Name the blood parasite species.
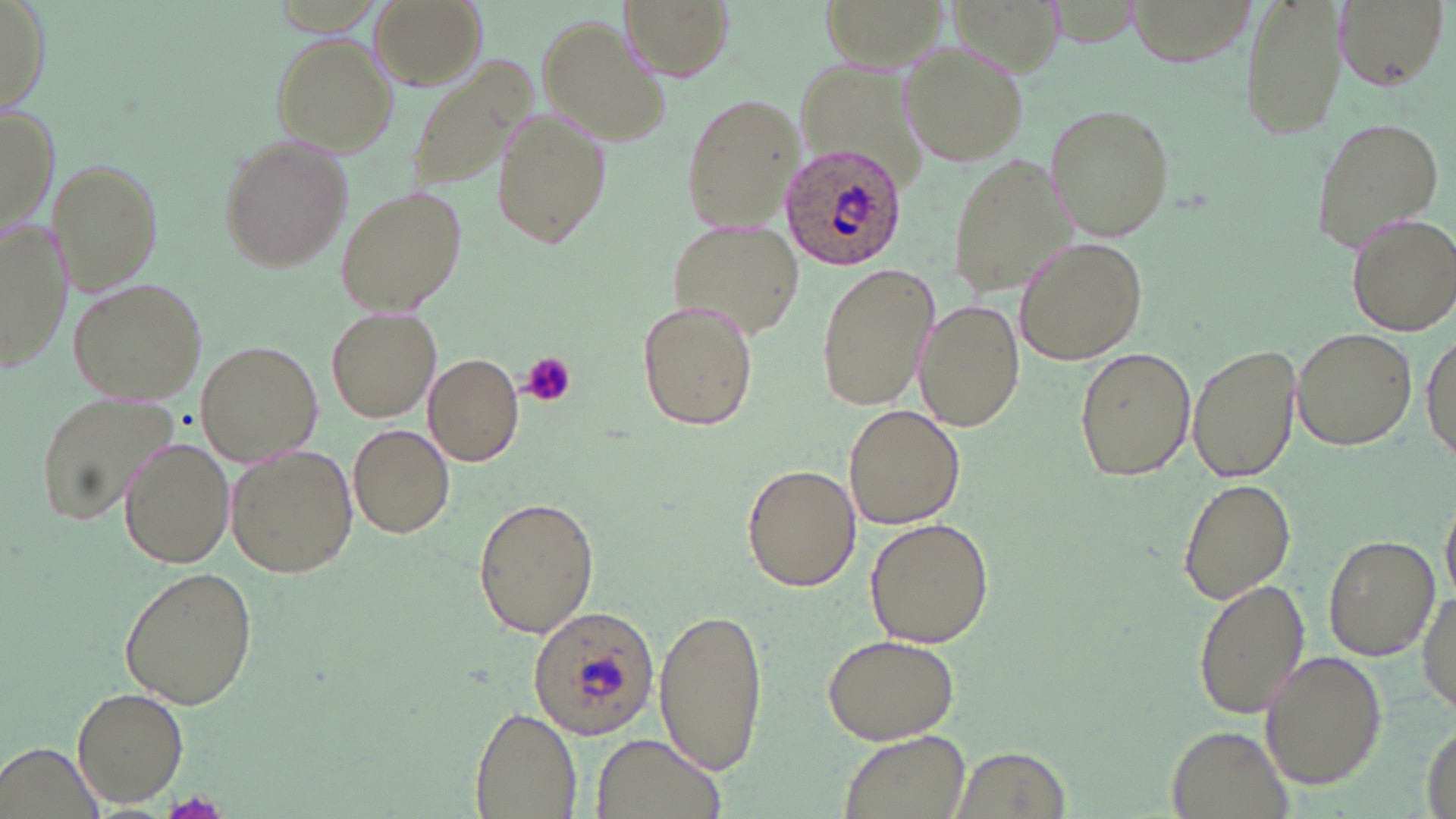
Plasmodium ovale.

magnification = 1000x
modality = light microscopy
platelet locations = approximate bounding boxes as (x1,y1)-(x2,y2) corner pairs in pixels: (521,352)-(576,408)
image size = 1456×819 pixels
stain = May-Grünwald-Giemsa
Plasmodium ovale-infected red blood cell locations = approximate bounding boxes as (x1,y1)-(x2,y2) corner pairs in pixels: (780,144)-(907,271), (526,605)-(658,738)
field of view = one of a larger specimen
uninfected red blood cell locations = approximate bounding boxes as (x1,y1)-(x2,y2) corner pairs in pixels: (369,0)-(484,91), (621,0)-(731,80), (822,0)-(951,69), (1238,0)-(1348,143), (1332,0)-(1449,91), (0,2)-(50,117), (540,15)-(669,142), (271,35)-(400,155), (897,40)-(1029,169), (794,58)-(928,169), (405,65)-(529,195), (681,94)-(803,233), (0,102)-(55,238), (1044,103)-(1175,242), (491,110)-(610,250), (1309,115)-(1443,252), (220,136)-(353,273), (948,151)-(1068,297), (51,160)-(162,295), (335,189)-(467,317), (1346,212)-(1456,334), (1,219)-(68,375), (669,221)-(808,339), (1015,236)-(1148,365), (815,262)-(939,410), (68,279)-(206,406), (915,299)-(1024,433), (637,300)-(759,432), (326,306)-(442,424), (1292,325)-(1419,451), (1421,329)-(1455,467), (197,341)-(323,467), (1188,342)-(1302,485), (1071,349)-(1198,481), (421,355)-(524,465), (39,390)-(180,527), (843,404)-(964,530), (348,424)-(456,539), (119,436)-(234,568), (225,444)-(358,579), (741,463)-(861,591), (1177,476)-(1297,608), (1442,491)-(1456,600), (473,495)-(597,640), (866,517)-(995,649), (1322,532)-(1440,663), (119,568)-(257,708), (1192,578)-(1309,720), (1418,581)-(1455,720), (653,604)-(767,776), (823,633)-(960,745), (1257,649)-(1388,791), (72,688)-(189,807), (470,707)-(581,819), (1166,726)-(1290,819), (838,730)-(970,819), (588,733)-(727,819), (1,738)-(108,818), (953,746)-(1069,817)
preparation = thin blood smear